Name the cell type shown.
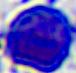

A leukocyte.

Summary:
  - Modality: micrograph
  - Magnification: 400x